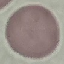
malaria_status: uninfected
image_type: cell patch, automatically extracted from a larger field of view and resized to 64 × 64 pixels
stain: Giemsa
capture: smartphone camera at the microscope eyepiece
preparation: thin blood smear